State the blood parasite species.
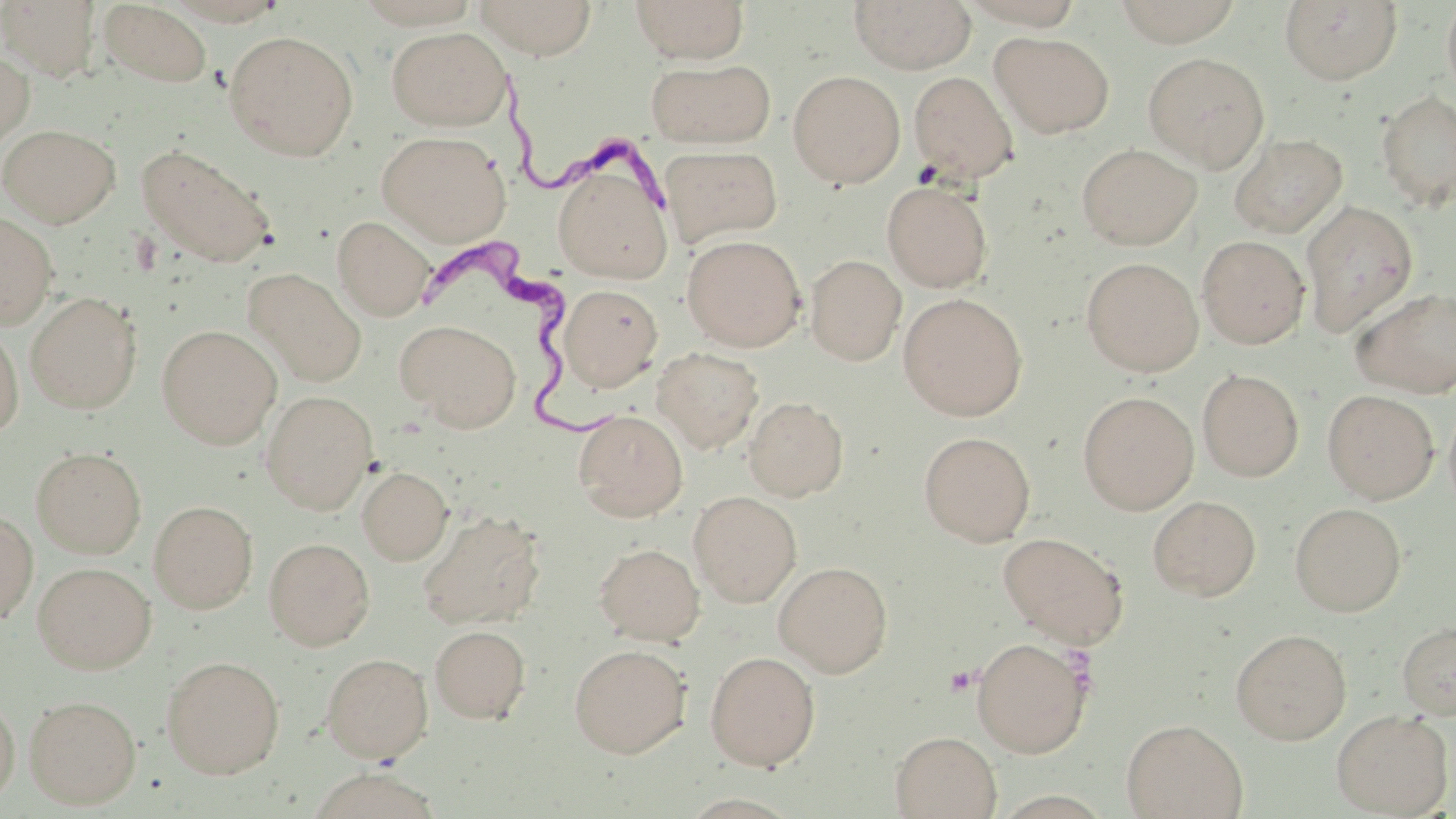

Trypanosoma brucei.

magnification: 1000x
trypanosoma_brucei_locations: 'approximate bounding boxes as [x1, y1, x2, y2] in pixels: [484, 65, 682, 212], [414, 236, 617, 447]'
stain: May-Grünwald-Giemsa
field_of_view: one of a larger specimen
uninfected_red_blood_cell_locations: 'approximate bounding boxes as [x1, y1, x2, y2] in pixels: [1, 0, 101, 81], [164, 0, 289, 26], [472, 0, 599, 59], [630, 0, 749, 63], [848, 0, 975, 74], [1112, 0, 1243, 46], [1279, 0, 1403, 85], [1441, 0, 1456, 104], [101, 2, 212, 87], [387, 27, 511, 131], [225, 30, 359, 160], [990, 31, 1115, 137], [0, 49, 35, 150], [1142, 52, 1269, 171], [647, 58, 776, 148], [788, 70, 905, 188], [909, 71, 1019, 182], [1376, 89, 1456, 213], [1, 124, 121, 227], [376, 131, 511, 245], [1228, 133, 1348, 238], [1077, 143, 1202, 250], [136, 144, 276, 267], [660, 145, 783, 246], [551, 156, 674, 284], [882, 181, 993, 292], [1300, 200, 1419, 337], [0, 212, 58, 328], [333, 216, 435, 321], [682, 235, 806, 351], [1197, 235, 1310, 348], [805, 255, 906, 365], [1081, 257, 1203, 376], [244, 268, 368, 388], [558, 284, 663, 391], [1350, 285, 1456, 398], [25, 291, 142, 414], [898, 293, 1027, 420], [396, 318, 522, 431], [0, 322, 24, 438], [157, 324, 282, 449], [652, 347, 764, 453], [1197, 368, 1304, 482], [1322, 389, 1439, 503], [260, 390, 378, 514], [1078, 391, 1199, 514], [743, 396, 848, 501], [574, 410, 688, 521], [919, 431, 1036, 545], [31, 447, 146, 558], [357, 466, 453, 564], [688, 491, 802, 607], [1148, 495, 1261, 600], [149, 500, 258, 613], [1289, 502, 1407, 617], [417, 509, 546, 629], [0, 510, 38, 625], [998, 531, 1129, 648], [264, 537, 374, 650], [594, 542, 705, 645], [774, 561, 893, 676], [33, 562, 156, 674], [1396, 621, 1456, 720], [429, 625, 530, 724], [1231, 628, 1351, 744], [972, 636, 1092, 758], [569, 643, 690, 757], [705, 651, 820, 770], [321, 652, 433, 762], [161, 655, 285, 779], [0, 693, 20, 807], [24, 694, 141, 808], [1330, 709, 1453, 817], [1121, 718, 1248, 818], [891, 731, 1002, 819], [304, 768, 444, 819]'
image_size: 1456×819 pixels
modality: optical microscopy
preparation: thin blood film